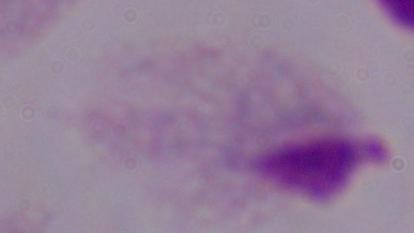

A trichomonad is shown. Micrograph. Captured at 1000x magnification.